Report the malaria status of this cell.
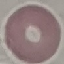
Uninfected.

Thin smear of blood. Giemsa stain. Automatically extracted cell patch, resized to 64 × 64 pixels. Photographed with a smartphone camera at the microscope eyepiece.